Locate every malaria parasite and identify its life-cycle stage.
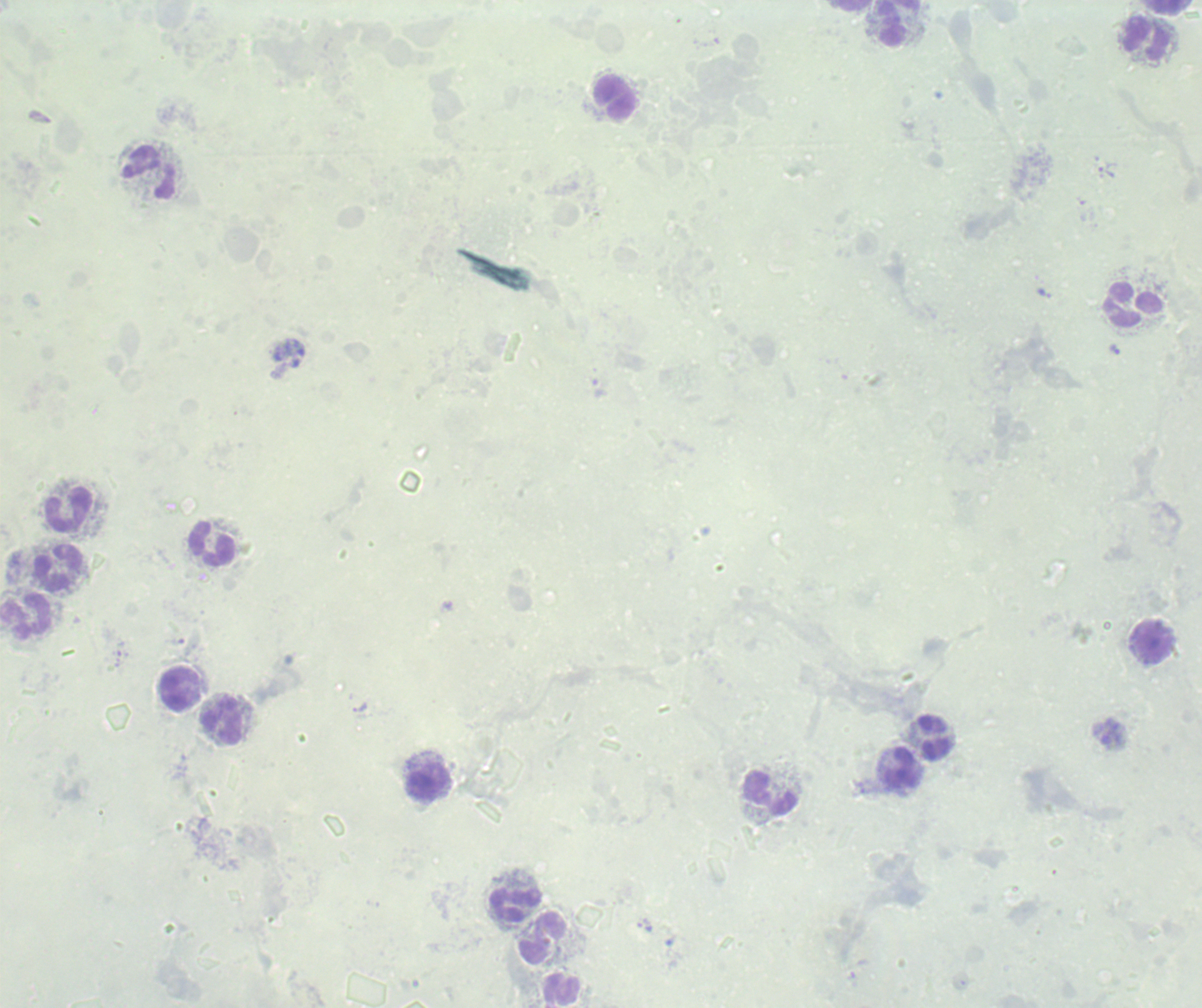
Approximate centers as [x, y] in pixels.
Trophozoites: [1106, 172], [1045, 293], [1114, 349], [359, 707].
No schizont or gametocyte forms observed.

Approximate centers as [x, y] in pixels. Leukocyte locations: [853, 5], [1164, 6], [892, 23], [1148, 38], [613, 98], [150, 173], [1134, 304], [69, 509], [213, 543], [59, 570], [25, 617], [1153, 642], [180, 688], [221, 721], [933, 736], [901, 768], [427, 780], [771, 793], [515, 906], [542, 936]. Captured at 100x magnification. Thick smear of blood. Previously used in a real diagnosis. Single field of view. Romanowsky-stained preparation. Image is 1202×1008 pixels. Background quality: unsatisfactory.